Point out each Plasmodium parasite.
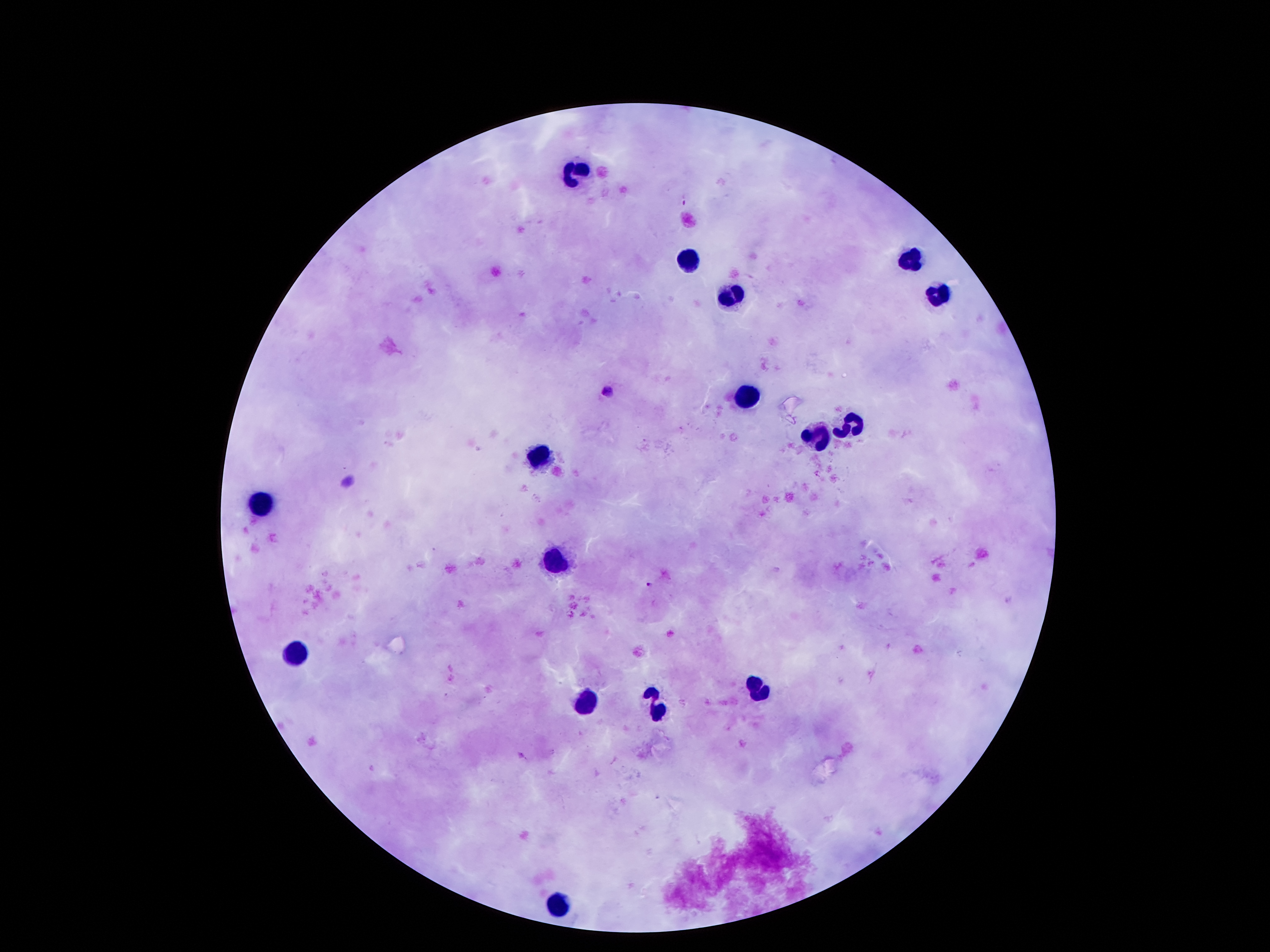
Approximate centers as [x, y] in pixels.
Plasmodium parasites: [684, 201], [606, 389], [648, 585].

leukocyte_locations: 'approximate centers as [x, y] in pixels: [577, 170], [913, 260], [690, 264], [936, 294], [732, 296], [745, 402], [854, 421], [823, 434], [539, 453], [262, 507], [556, 560], [298, 653], [760, 689], [585, 702], [657, 709], [560, 907]'
field_of_view: single
image_size: 1270×952 pixels
preparation: thick blood smear
magnification: 100x
stain: Giemsa
capture: smartphone through the microscope eyepiece
patient_malaria_status: positive for Plasmodium falciparum